Comment on the morphology of the red blood cells.
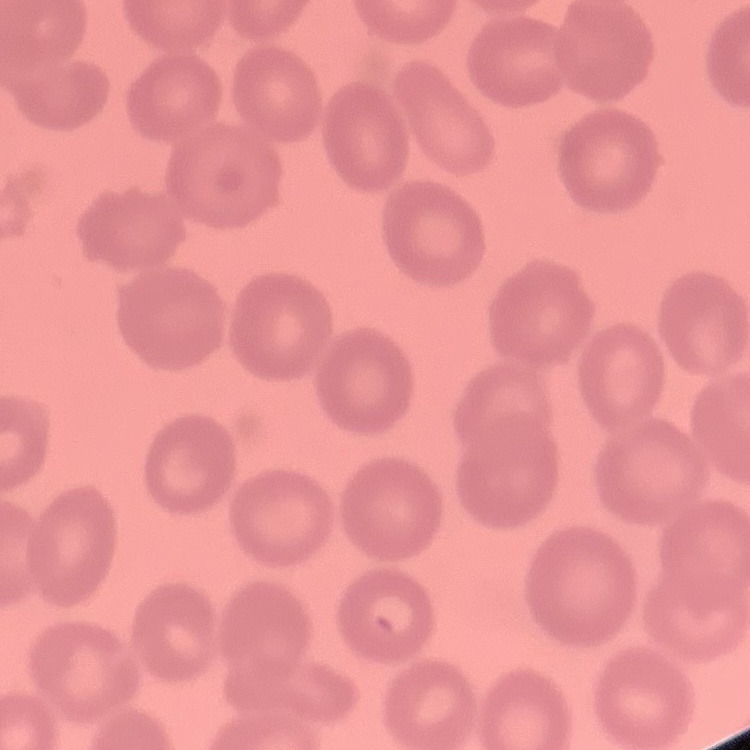
They show no rouleaux formation.

image type = square crop of a larger photomicrograph
preparation = thin blood smear
stain = Field's or Giemsa